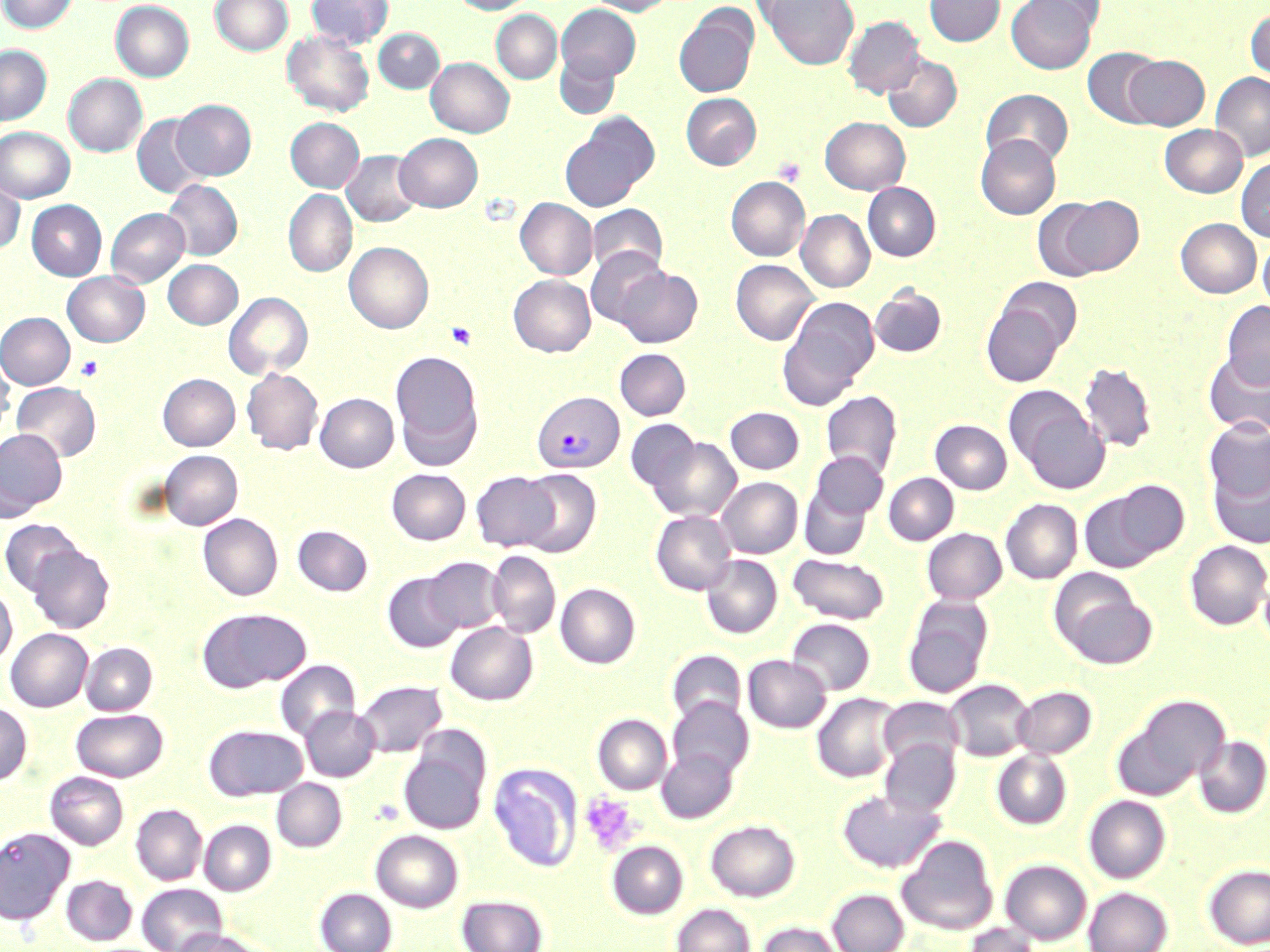
slide-level diagnosis = Plasmodium vivax
image size = 1270×952 pixels
uninfected red blood cell locations = approximate bounding boxes as (x1,y1)-(x2,y2) corner pairs in pixels: (0,0)-(76,34), (210,0)-(293,56), (307,0)-(393,49), (452,0)-(536,15), (586,0)-(674,16), (747,0)-(832,27), (761,0)-(858,69), (924,0)-(1005,46), (1029,0)-(1106,35), (110,1)-(194,82), (1006,1)-(1097,74), (556,4)-(641,83), (674,6)-(759,98), (1246,7)-(1270,84), (491,11)-(561,84), (765,11)-(924,88), (844,15)-(924,98), (374,29)-(445,93), (282,30)-(374,117), (0,45)-(51,125), (1082,48)-(1164,128), (883,52)-(961,132), (555,53)-(620,120), (1123,55)-(1209,130), (426,57)-(514,138), (1210,72)-(1270,161), (63,74)-(148,157), (981,89)-(1073,168), (681,93)-(761,170), (171,100)-(256,180), (132,115)-(208,198), (559,116)-(657,212), (820,116)-(910,194), (286,117)-(364,192), (1160,124)-(1247,197), (0,127)-(74,203), (394,133)-(483,212), (976,134)-(1061,219), (342,151)-(423,227), (1236,157)-(1270,242), (0,175)-(25,254), (726,177)-(809,261), (163,180)-(242,260), (863,183)-(940,261), (283,189)-(357,277), (1054,195)-(1144,277), (515,198)-(597,280), (27,200)-(107,280), (588,203)-(668,278), (106,208)-(190,287), (796,210)-(875,292), (1176,218)-(1261,298), (1258,237)-(1270,314), (344,242)-(433,333), (585,248)-(668,329), (163,259)-(243,329), (731,260)-(818,345), (614,266)-(702,347), (62,271)-(149,347), (508,274)-(595,357), (998,277)-(1083,353), (870,285)-(947,357), (224,292)-(312,380), (778,298)-(878,408), (1222,301)-(1270,389), (982,303)-(1065,386), (0,312)-(75,390), (614,348)-(691,420), (391,349)-(484,467), (1203,351)-(1270,436), (0,353)-(15,436), (1079,362)-(1157,453), (242,368)-(323,455), (158,373)-(240,450), (11,382)-(101,462), (1008,390)-(1109,494), (821,391)-(902,478), (315,393)-(399,472), (725,407)-(804,474), (625,419)-(701,496), (1204,419)-(1270,503), (931,420)-(1012,494), (0,428)-(66,518), (648,436)-(741,523), (160,450)-(242,530), (811,451)-(888,520), (1208,461)-(1270,549), (387,468)-(470,545), (516,469)-(602,558), (471,471)-(560,551), (884,473)-(958,545), (717,477)-(802,558), (1108,479)-(1189,560), (799,485)-(872,560), (1079,490)-(1164,573), (1001,499)-(1082,584), (651,510)-(736,595), (198,513)-(283,601), (0,519)-(83,596), (293,525)-(373,596), (922,528)-(1006,604), (1185,540)-(1270,630), (26,543)-(115,633), (487,550)-(560,638), (788,553)-(890,624), (701,555)-(782,638), (424,557)-(504,634), (383,572)-(464,652), (1054,576)-(1156,669), (555,583)-(640,668), (0,584)-(17,666), (903,596)-(994,698), (197,607)-(311,692), (787,618)-(875,695), (446,622)-(537,705), (6,628)-(92,712), (80,642)-(157,715), (667,649)-(746,728), (743,655)-(830,733), (275,660)-(360,741), (946,679)-(1033,761), (356,680)-(446,757), (1013,686)-(1096,758), (812,693)-(901,783), (1120,695)-(1229,794), (879,696)-(965,769), (668,697)-(753,781), (0,702)-(32,784), (300,706)-(380,781), (72,709)-(168,781), (593,714)-(671,795), (204,724)-(308,801), (1194,736)-(1270,818), (399,739)-(490,834), (879,740)-(960,818), (657,749)-(738,823), (992,750)-(1071,829), (489,763)-(582,872), (45,771)-(128,849), (272,778)-(346,851), (837,789)-(945,874), (1084,795)-(1170,883), (131,804)-(207,885), (199,819)-(275,895), (705,820)-(800,901), (0,827)-(74,924), (371,830)-(463,912), (897,835)-(998,935), (607,841)-(687,919), (1001,859)-(1091,944), (1204,864)-(1270,948), (61,874)-(137,945), (138,883)-(227,952), (1084,887)-(1172,952), (315,888)-(397,952), (828,889)-(909,952), (457,895)-(547,952), (672,904)-(755,952), (757,921)-(842,952), (963,923)-(1042,952), (172,929)-(272,952)
Plasmodium vivax-infected red blood cell locations = approximate bounding boxes as (x1,y1)-(x2,y2) corner pairs in pixels: (533,391)-(623,474)
modality = light microscopy
platelet locations = approximate bounding boxes as (x1,y1)-(x2,y2) corner pairs in pixels: (772,157)-(806,186), (445,321)-(478,350), (75,356)-(104,381), (580,793)-(640,855)
field of view = one of a larger specimen
magnification = 1000x
preparation = thin blood film
stain = May-Grünwald-Giemsa